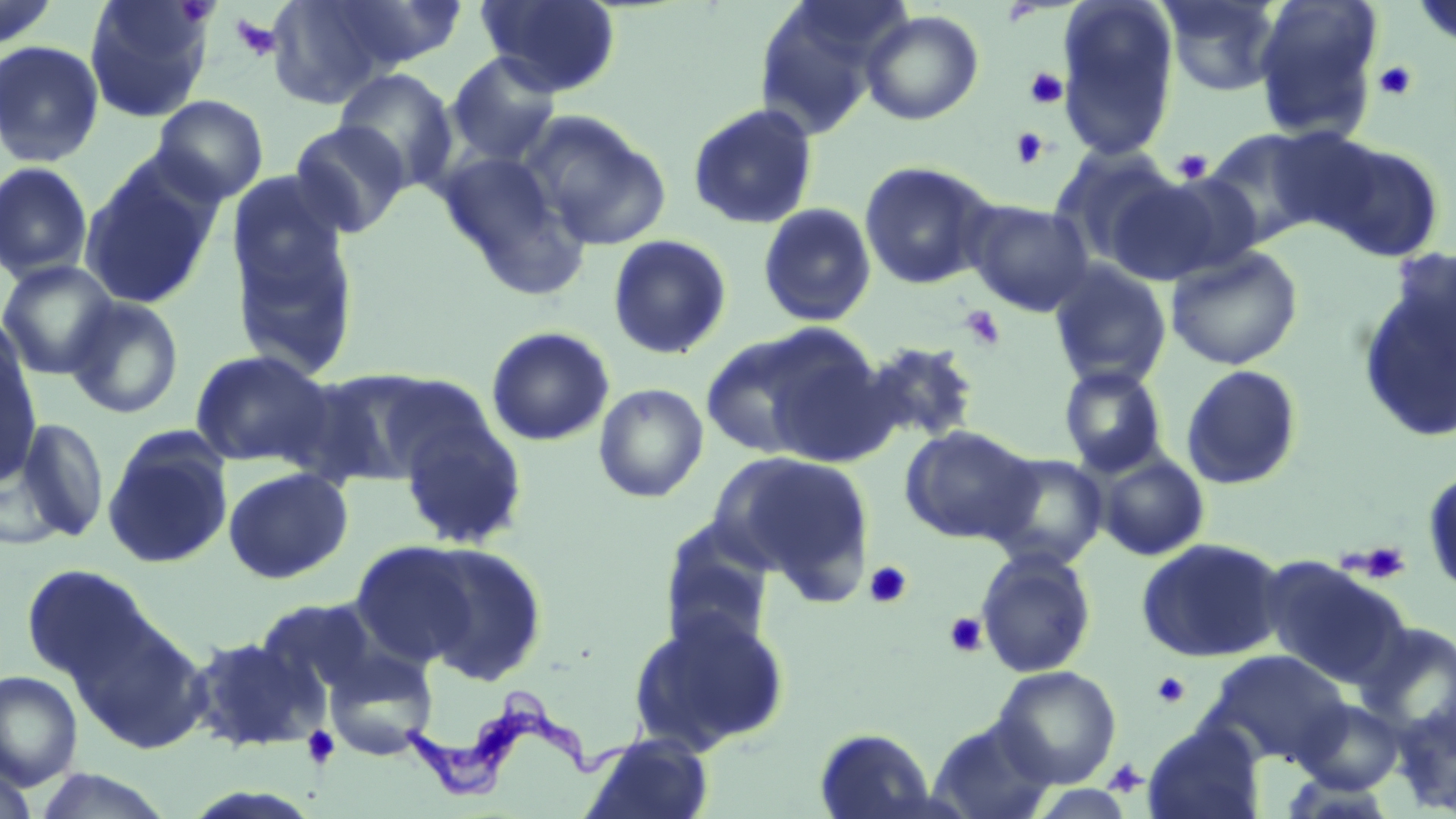
Approximate bounding boxes as named x1/y1/x2/y2 corners in pixels. Trypanosoma brucei locations: (x1=397, y1=694, x2=654, y2=801). Uninfected red blood cell locations: (x1=0, y1=0, x2=61, y2=49), (x1=83, y1=0, x2=214, y2=123), (x1=266, y1=0, x2=401, y2=108), (x1=479, y1=0, x2=621, y2=97), (x1=751, y1=0, x2=904, y2=136), (x1=1159, y1=0, x2=1284, y2=98), (x1=1252, y1=0, x2=1383, y2=142), (x1=1412, y1=0, x2=1456, y2=50), (x1=319, y1=1, x2=470, y2=74), (x1=1056, y1=2, x2=1180, y2=162), (x1=861, y1=10, x2=984, y2=125), (x1=0, y1=39, x2=105, y2=167), (x1=445, y1=51, x2=562, y2=167), (x1=333, y1=68, x2=460, y2=193), (x1=152, y1=94, x2=269, y2=205), (x1=687, y1=102, x2=819, y2=230), (x1=519, y1=110, x2=671, y2=249), (x1=288, y1=121, x2=411, y2=238), (x1=1202, y1=128, x2=1335, y2=246), (x1=1318, y1=140, x2=1446, y2=263), (x1=1050, y1=147, x2=1180, y2=266), (x1=437, y1=150, x2=587, y2=295), (x1=80, y1=157, x2=223, y2=310), (x1=858, y1=159, x2=998, y2=291), (x1=0, y1=162, x2=94, y2=283), (x1=1149, y1=173, x2=1266, y2=276), (x1=1102, y1=176, x2=1226, y2=285), (x1=228, y1=196, x2=361, y2=381), (x1=964, y1=199, x2=1095, y2=316), (x1=758, y1=202, x2=877, y2=327), (x1=606, y1=234, x2=733, y2=360), (x1=1165, y1=246, x2=1304, y2=370), (x1=1357, y1=259, x2=1456, y2=446), (x1=0, y1=260, x2=119, y2=380), (x1=1048, y1=262, x2=1172, y2=390), (x1=65, y1=296, x2=184, y2=420), (x1=486, y1=326, x2=615, y2=446), (x1=700, y1=326, x2=866, y2=461), (x1=0, y1=331, x2=43, y2=486), (x1=854, y1=340, x2=982, y2=448), (x1=190, y1=349, x2=334, y2=468), (x1=1180, y1=364, x2=1304, y2=490), (x1=1058, y1=365, x2=1169, y2=477), (x1=292, y1=367, x2=447, y2=488), (x1=592, y1=383, x2=710, y2=503), (x1=396, y1=414, x2=528, y2=550), (x1=13, y1=415, x2=110, y2=542), (x1=899, y1=424, x2=1038, y2=544), (x1=102, y1=428, x2=234, y2=569), (x1=714, y1=451, x2=874, y2=592), (x1=983, y1=452, x2=1109, y2=571), (x1=1095, y1=452, x2=1210, y2=561), (x1=223, y1=466, x2=353, y2=583), (x1=1422, y1=467, x2=1455, y2=598), (x1=658, y1=522, x2=778, y2=649), (x1=1135, y1=537, x2=1286, y2=663), (x1=350, y1=540, x2=479, y2=666), (x1=415, y1=542, x2=549, y2=686), (x1=975, y1=548, x2=1097, y2=678), (x1=1261, y1=556, x2=1412, y2=688), (x1=21, y1=563, x2=152, y2=682), (x1=255, y1=599, x2=377, y2=698), (x1=627, y1=608, x2=790, y2=755), (x1=83, y1=616, x2=211, y2=755), (x1=188, y1=635, x2=324, y2=753), (x1=324, y1=649, x2=438, y2=760), (x1=1206, y1=650, x2=1351, y2=768), (x1=992, y1=665, x2=1122, y2=788), (x1=0, y1=671, x2=83, y2=790), (x1=1293, y1=699, x2=1405, y2=794), (x1=1392, y1=702, x2=1456, y2=815), (x1=928, y1=718, x2=1057, y2=819), (x1=1143, y1=723, x2=1265, y2=819), (x1=815, y1=727, x2=939, y2=818), (x1=584, y1=732, x2=714, y2=819), (x1=0, y1=763, x2=39, y2=819), (x1=30, y1=768, x2=175, y2=818). Platelet locations: (x1=230, y1=15, x2=282, y2=61), (x1=1373, y1=60, x2=1418, y2=102), (x1=1024, y1=67, x2=1068, y2=109), (x1=1010, y1=128, x2=1050, y2=169), (x1=1171, y1=149, x2=1213, y2=184), (x1=959, y1=305, x2=1006, y2=351), (x1=1351, y1=541, x2=1411, y2=583), (x1=864, y1=560, x2=913, y2=609), (x1=944, y1=612, x2=987, y2=657), (x1=1151, y1=671, x2=1192, y2=709), (x1=301, y1=725, x2=341, y2=769), (x1=1103, y1=759, x2=1148, y2=798). Slide-level diagnosis: Trypanosoma brucei. Captured at 1000x magnification. Light microscopy. May-Grünwald-Giemsa-stained preparation. One field of a larger specimen. Thin blood smear. Image is 1456×819 pixels.